Identify the parasite.
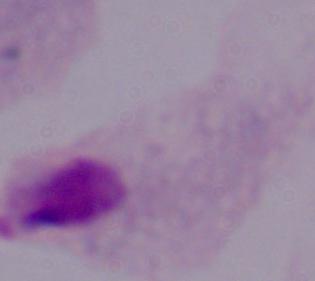

A trichomonad.

magnification = 1000x
modality = photomicrograph